Assess the morphology of the erythrocytes.
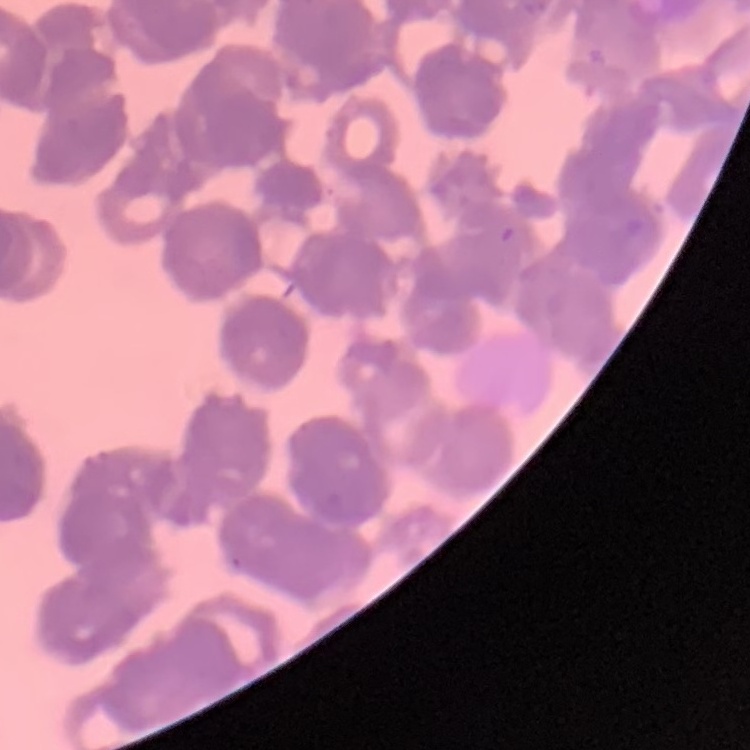

They show rouleaux formation.

preparation = thin blood smear
stain = Field's or Giemsa
image type = square crop of a larger photomicrograph